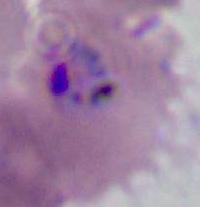 400x or 1000x magnification. Photomicrograph. A Plasmodium parasite is shown.